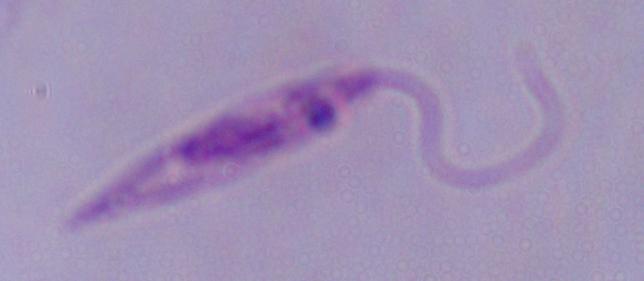 A Leishmania parasite is shown. Micrograph. Captured at 1000x magnification.